Report the malaria status of this cell.
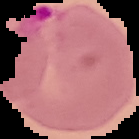

It is parasitized.

image type = segmented cell region with the area outside set to black
image size = 139×139 pixels
preparation = thin blood smear